State which parasite is depicted.
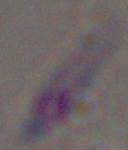
Toxoplasma gondii.

Micrograph. Captured at 1000x magnification.